Classify this cell by malaria status.
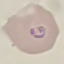

It is parasitized.

Summary:
  - Preparation: thin smear
  - Stain: Giemsa
  - Image type: cell patch, automatically extracted from a larger field of view and resized to 64 × 64 pixels
  - Capture: smartphone camera at the microscope eyepiece